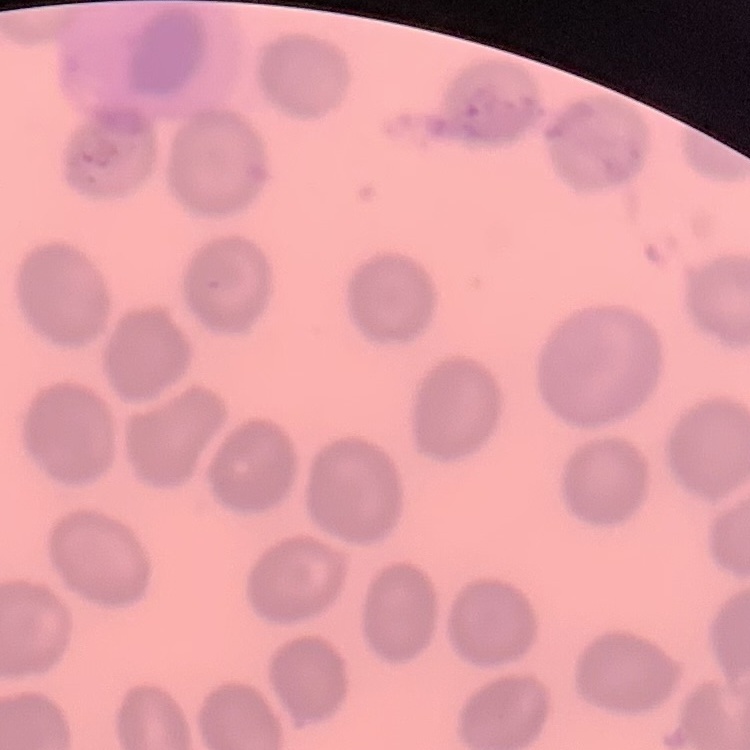
Summary:
  - Erythrocyte morphology: no rouleaux formation
  - Stain: Field's or Giemsa
  - Preparation: thin blood film
  - Image type: one tile cut from a larger photomicrograph